Assess the morphology of the red blood cells.
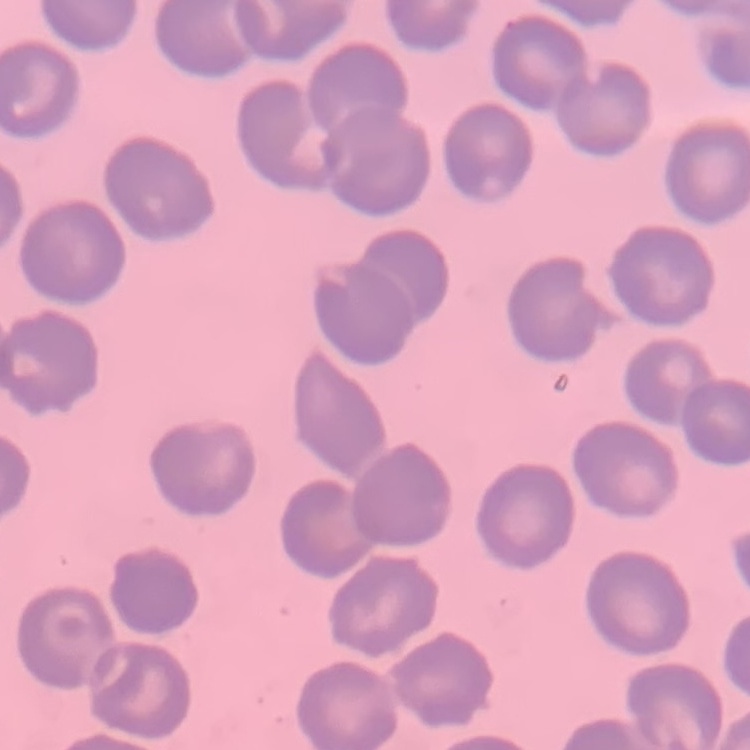
No rouleaux formation.

image type = one tile cut from a larger photomicrograph
stain = Field's or Giemsa
preparation = thin peripheral smear